Look for Plasmodium parasites.
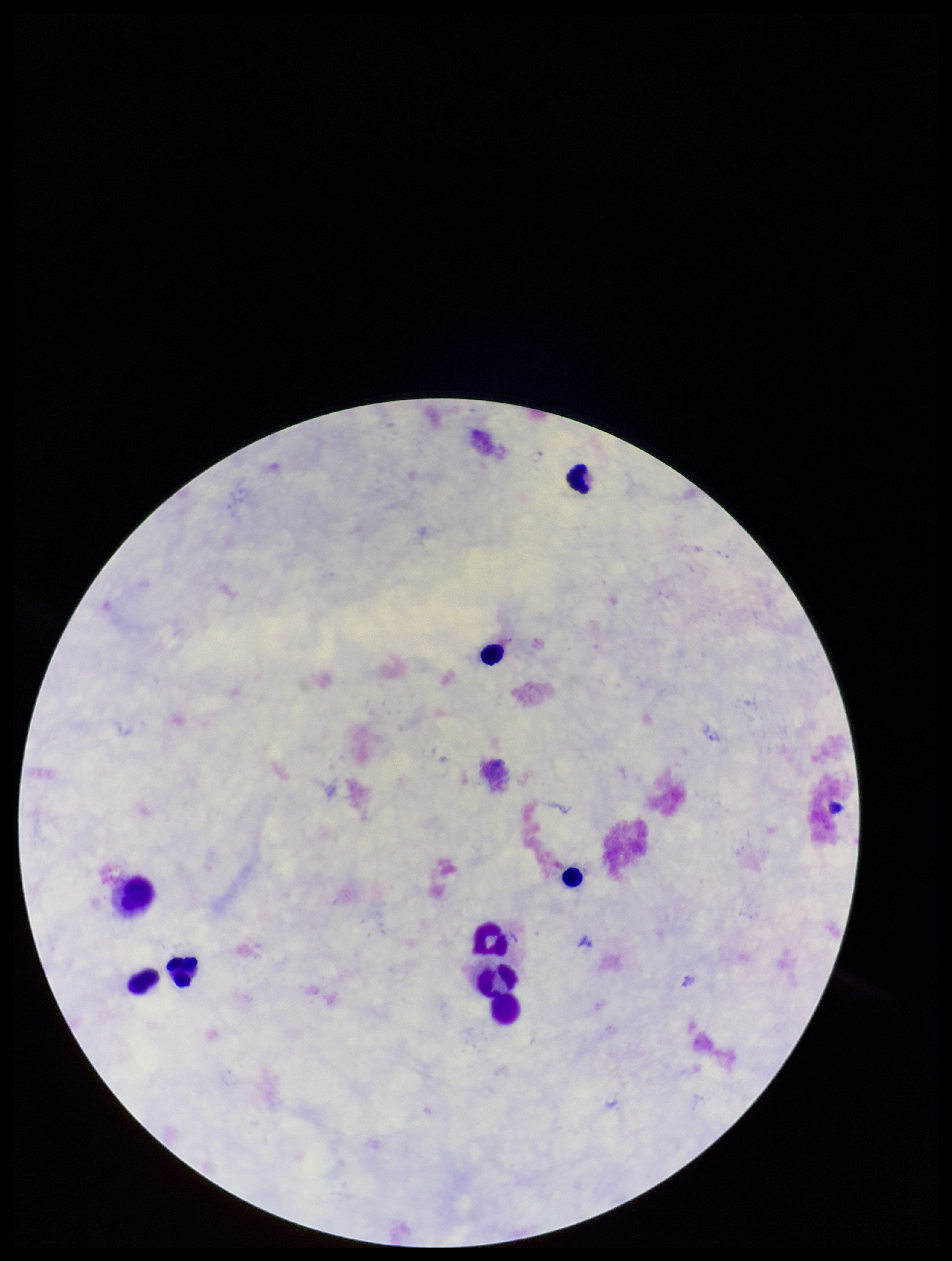
None detected.

Image is 952×1261 pixels. Parasite count: 0. Patient malaria status: negative. Preparation: thick blood smear. Leukocyte count: 9. Smartphone photograph taken through the eyepiece of a microscope. Single field of view. Stained with Giemsa.